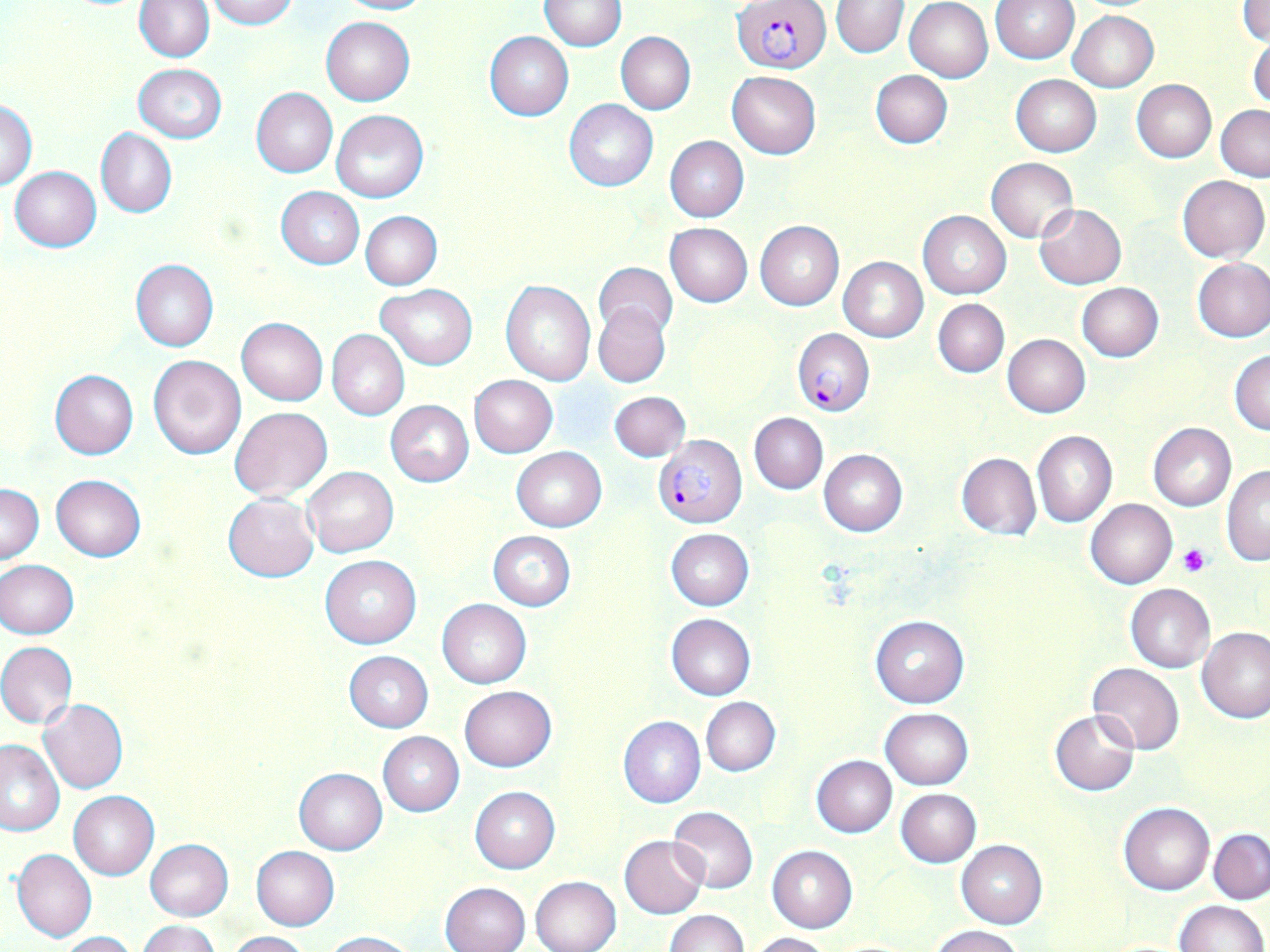
Summary:
  - Coordinate format: approximate bounding boxes as named x1/y1/x2/y2 corners in pixels
  - Plasmodium falciparum-infected red blood cell locations: (x1=734, y1=2, x2=832, y2=73), (x1=792, y1=327, x2=875, y2=415), (x1=653, y1=435, x2=745, y2=526)
  - Uninfected red blood cell locations: (x1=206, y1=0, x2=297, y2=28), (x1=335, y1=0, x2=433, y2=15), (x1=990, y1=0, x2=1079, y2=63), (x1=1239, y1=0, x2=1270, y2=45), (x1=135, y1=1, x2=214, y2=61), (x1=540, y1=1, x2=627, y2=50), (x1=831, y1=1, x2=908, y2=58), (x1=904, y1=1, x2=993, y2=83), (x1=1068, y1=11, x2=1158, y2=92), (x1=321, y1=16, x2=414, y2=105), (x1=485, y1=31, x2=573, y2=120), (x1=616, y1=32, x2=695, y2=113), (x1=1248, y1=34, x2=1270, y2=114), (x1=133, y1=64, x2=226, y2=142), (x1=870, y1=70, x2=952, y2=148), (x1=728, y1=71, x2=821, y2=158), (x1=1005, y1=72, x2=1093, y2=237), (x1=1011, y1=74, x2=1101, y2=155), (x1=1131, y1=80, x2=1216, y2=163), (x1=251, y1=87, x2=337, y2=177), (x1=0, y1=99, x2=37, y2=190), (x1=564, y1=99, x2=658, y2=191), (x1=1217, y1=106, x2=1270, y2=181), (x1=330, y1=109, x2=428, y2=202), (x1=96, y1=128, x2=177, y2=218), (x1=665, y1=136, x2=749, y2=222), (x1=986, y1=157, x2=1079, y2=243), (x1=10, y1=166, x2=101, y2=250), (x1=1177, y1=175, x2=1269, y2=263), (x1=276, y1=186, x2=364, y2=269), (x1=1034, y1=204, x2=1127, y2=289), (x1=361, y1=211, x2=442, y2=289), (x1=919, y1=211, x2=1011, y2=298), (x1=755, y1=220, x2=844, y2=310), (x1=665, y1=223, x2=753, y2=307), (x1=838, y1=256, x2=928, y2=342), (x1=1193, y1=257, x2=1270, y2=342), (x1=130, y1=259, x2=219, y2=351), (x1=595, y1=263, x2=677, y2=339), (x1=501, y1=280, x2=595, y2=384), (x1=1076, y1=282, x2=1163, y2=361), (x1=376, y1=284, x2=476, y2=370), (x1=934, y1=299, x2=1009, y2=377), (x1=593, y1=302, x2=670, y2=388), (x1=237, y1=317, x2=327, y2=405), (x1=327, y1=329, x2=409, y2=420), (x1=1002, y1=334, x2=1090, y2=417), (x1=1230, y1=349, x2=1270, y2=435), (x1=149, y1=355, x2=245, y2=458), (x1=49, y1=370, x2=139, y2=458), (x1=468, y1=375, x2=557, y2=458), (x1=609, y1=391, x2=690, y2=461), (x1=385, y1=401, x2=474, y2=485), (x1=230, y1=406, x2=333, y2=500), (x1=749, y1=412, x2=828, y2=494), (x1=1148, y1=423, x2=1236, y2=511), (x1=1032, y1=431, x2=1117, y2=528), (x1=512, y1=447, x2=606, y2=531), (x1=818, y1=449, x2=906, y2=537), (x1=955, y1=452, x2=1040, y2=540), (x1=303, y1=466, x2=398, y2=557), (x1=1221, y1=466, x2=1270, y2=564), (x1=52, y1=474, x2=145, y2=562), (x1=0, y1=484, x2=44, y2=564), (x1=223, y1=493, x2=319, y2=581), (x1=1086, y1=498, x2=1177, y2=589), (x1=666, y1=528, x2=754, y2=610), (x1=486, y1=530, x2=576, y2=611), (x1=320, y1=555, x2=421, y2=648), (x1=0, y1=560, x2=79, y2=637), (x1=1125, y1=584, x2=1215, y2=673), (x1=436, y1=598, x2=532, y2=688), (x1=666, y1=614, x2=755, y2=700), (x1=870, y1=616, x2=969, y2=707), (x1=1197, y1=627, x2=1269, y2=723), (x1=0, y1=642, x2=77, y2=728), (x1=344, y1=651, x2=432, y2=732), (x1=1089, y1=662, x2=1184, y2=754), (x1=460, y1=687, x2=556, y2=770), (x1=701, y1=696, x2=780, y2=776), (x1=38, y1=698, x2=128, y2=794), (x1=880, y1=708, x2=972, y2=790), (x1=1049, y1=710, x2=1141, y2=795), (x1=618, y1=716, x2=705, y2=808), (x1=378, y1=731, x2=464, y2=816), (x1=0, y1=740, x2=64, y2=835), (x1=811, y1=756, x2=896, y2=837), (x1=292, y1=767, x2=388, y2=855), (x1=470, y1=786, x2=559, y2=873), (x1=895, y1=788, x2=981, y2=866), (x1=69, y1=791, x2=159, y2=881), (x1=1118, y1=802, x2=1215, y2=895), (x1=667, y1=807, x2=758, y2=893), (x1=1209, y1=829, x2=1269, y2=904), (x1=620, y1=835, x2=707, y2=918), (x1=145, y1=839, x2=233, y2=920), (x1=957, y1=840, x2=1047, y2=928), (x1=251, y1=845, x2=339, y2=930), (x1=767, y1=845, x2=858, y2=932), (x1=12, y1=847, x2=96, y2=942), (x1=531, y1=876, x2=620, y2=952), (x1=441, y1=882, x2=530, y2=952), (x1=1173, y1=900, x2=1267, y2=952), (x1=665, y1=911, x2=747, y2=952), (x1=136, y1=919, x2=220, y2=952), (x1=929, y1=925, x2=1026, y2=952), (x1=324, y1=930, x2=420, y2=952), (x1=57, y1=931, x2=136, y2=952), (x1=227, y1=931, x2=309, y2=951), (x1=750, y1=932, x2=831, y2=952)
  - Platelet locations: (x1=1179, y1=544, x2=1212, y2=576)
  - Slide-level diagnosis: Plasmodium falciparum
  - Field of view: one of a larger specimen
  - Stain: May-Grünwald-Giemsa
  - Magnification: 1000x
  - Preparation: thin blood smear
  - Image size: 1270×952 pixels
  - Modality: light microscopy